Name the parasite shown.
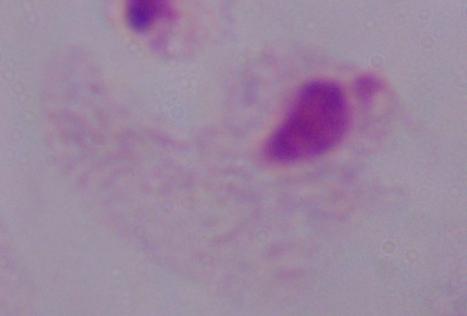

A trichomonad.

Captured at 1000x magnification. Photomicrograph.